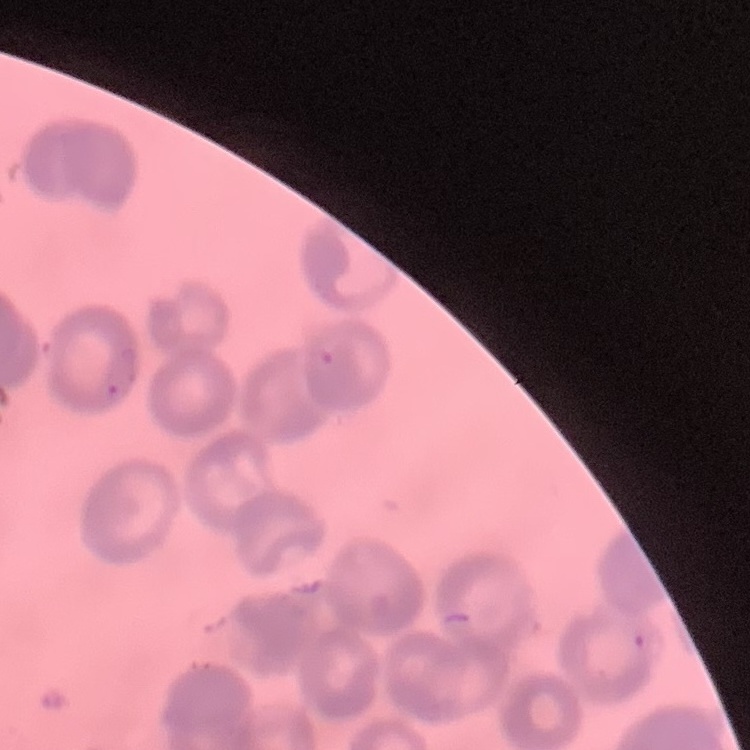
Summary:
  - Red blood cell morphology: rouleaux formation
  - Stain: Field's or Giemsa
  - Image type: square crop of a larger photomicrograph
  - Preparation: thin blood smear